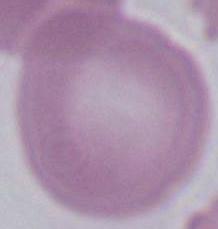

identification = erythrocyte
magnification = 1000x
modality = micrograph